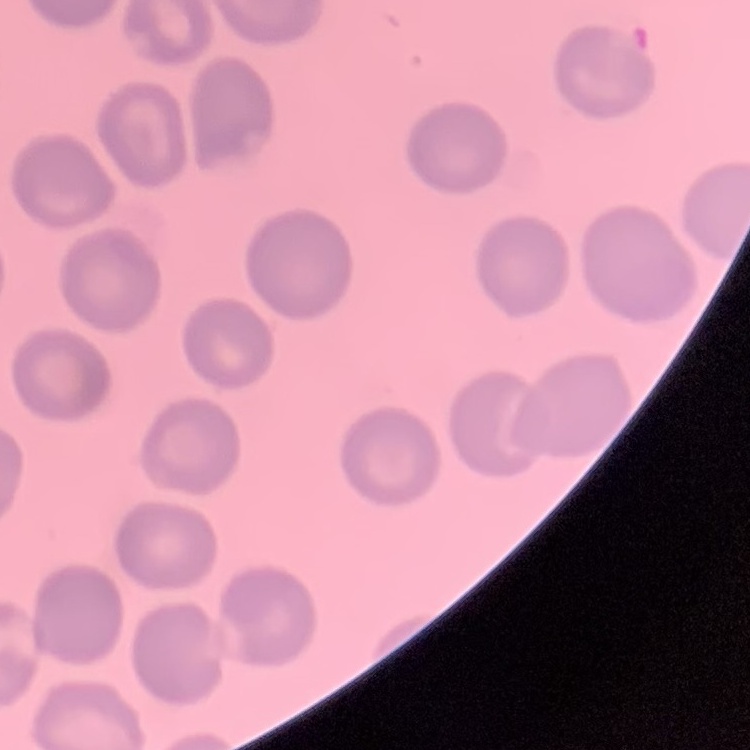

Summary:
  - Erythrocyte morphology: no rouleaux formation
  - Stain: Field's or Giemsa
  - Image type: one tile cut from a larger photomicrograph
  - Preparation: thin blood film